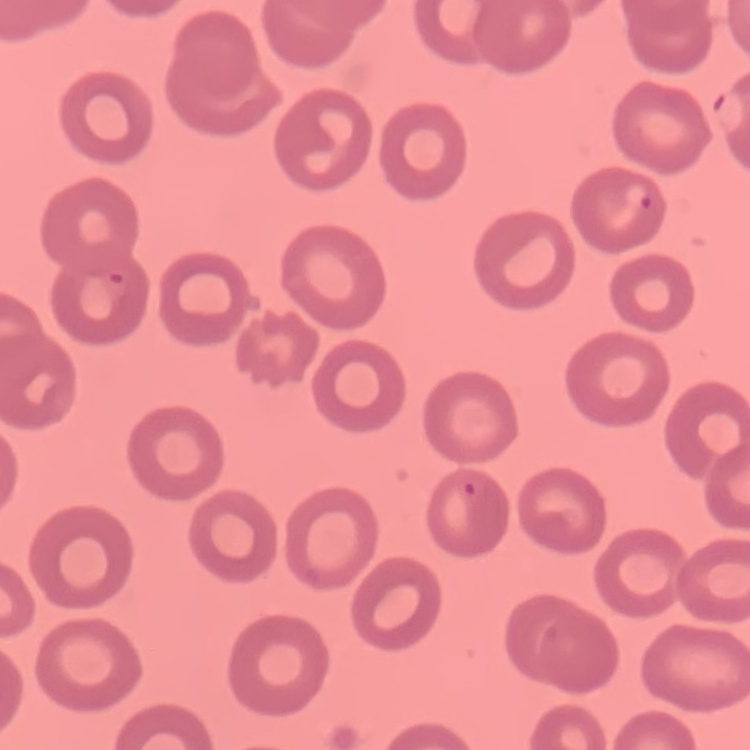

red blood cell morphology = no rouleaux formation
preparation = thin blood smear
image type = one tile cut from a larger photomicrograph
stain = Field's or Giemsa